Locate every Plasmodium parasite.
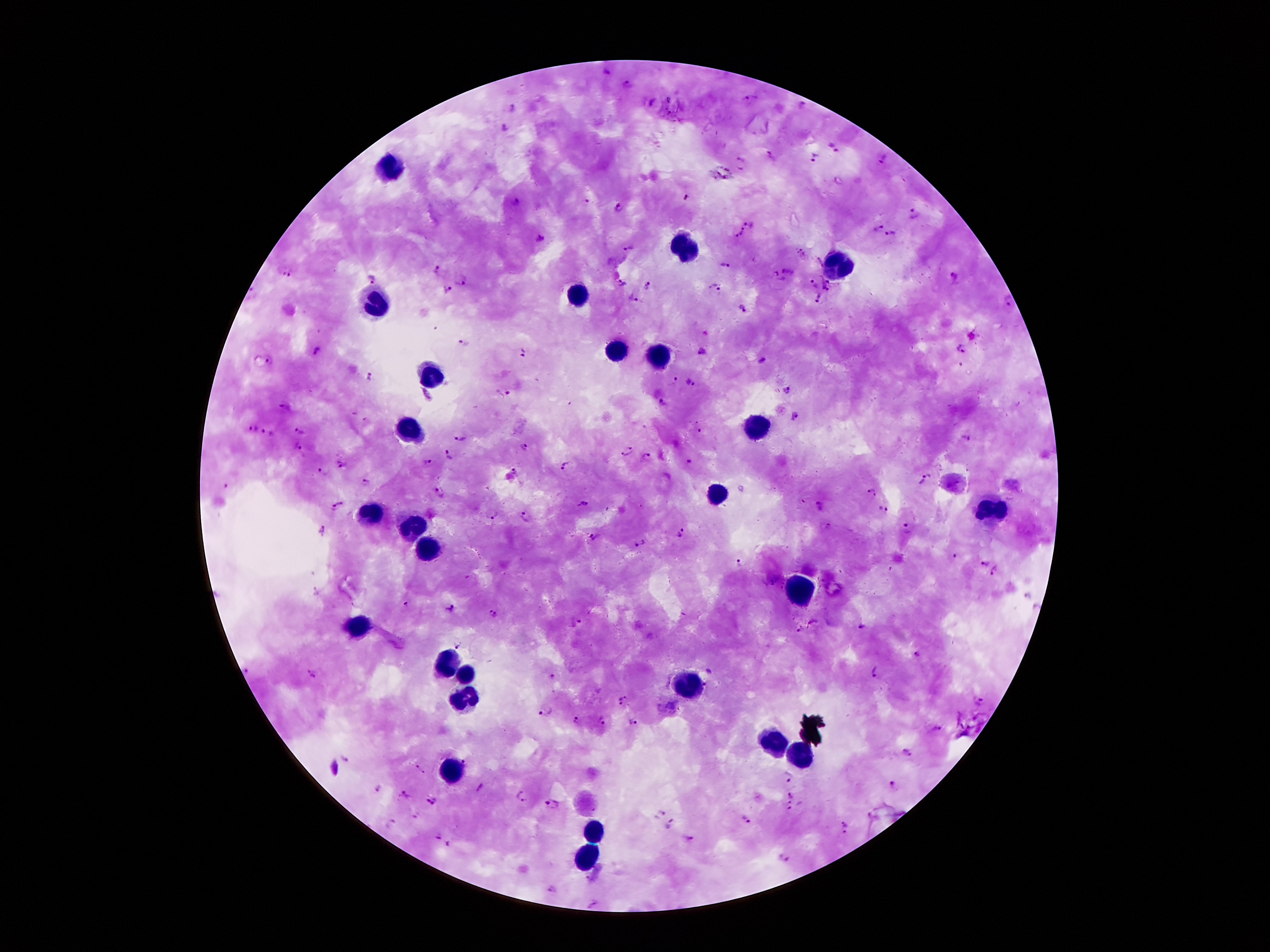

Approximate object centers, in pixels from the top-left corner.
Plasmodium parasites: (x=606, y=74), (x=627, y=85), (x=752, y=101), (x=511, y=107), (x=802, y=107), (x=504, y=127), (x=832, y=147), (x=770, y=154), (x=741, y=158), (x=815, y=160), (x=884, y=161), (x=585, y=201), (x=514, y=202), (x=619, y=209), (x=913, y=213), (x=750, y=225), (x=879, y=228), (x=741, y=233), (x=890, y=235), (x=538, y=238), (x=628, y=245), (x=723, y=267), (x=438, y=271), (x=284, y=273), (x=954, y=277), (x=779, y=278), (x=371, y=279), (x=461, y=281), (x=824, y=281), (x=621, y=282), (x=647, y=284), (x=812, y=284), (x=716, y=286), (x=448, y=290), (x=824, y=292), (x=634, y=299), (x=819, y=301), (x=1009, y=302), (x=744, y=307), (x=465, y=344), (x=963, y=349), (x=316, y=352), (x=701, y=352), (x=519, y=354), (x=269, y=362), (x=762, y=363), (x=371, y=378), (x=675, y=381), (x=691, y=384), (x=787, y=389), (x=502, y=391), (x=283, y=405), (x=356, y=412), (x=795, y=415), (x=367, y=422), (x=252, y=430), (x=300, y=432), (x=266, y=434), (x=459, y=438), (x=967, y=438), (x=633, y=446), (x=297, y=447), (x=526, y=447), (x=624, y=455), (x=449, y=456), (x=645, y=457), (x=427, y=463), (x=687, y=463), (x=340, y=464), (x=566, y=468), (x=516, y=470), (x=322, y=471), (x=925, y=479), (x=366, y=481), (x=440, y=492), (x=872, y=493), (x=342, y=501), (x=583, y=504), (x=822, y=505), (x=332, y=508), (x=883, y=509), (x=492, y=516), (x=526, y=516), (x=909, y=527), (x=323, y=532), (x=679, y=534), (x=594, y=536), (x=642, y=543), (x=955, y=557), (x=987, y=563), (x=739, y=566), (x=995, y=571), (x=405, y=605), (x=451, y=608), (x=493, y=616), (x=580, y=622), (x=814, y=622), (x=860, y=627), (x=797, y=629), (x=461, y=645), (x=916, y=653), (x=246, y=671), (x=877, y=672), (x=313, y=673), (x=551, y=677), (x=705, y=683), (x=622, y=700), (x=980, y=700), (x=545, y=711), (x=601, y=721), (x=576, y=722), (x=633, y=723), (x=936, y=727), (x=906, y=754), (x=346, y=759), (x=466, y=762), (x=421, y=769), (x=787, y=776), (x=378, y=787), (x=893, y=787), (x=479, y=788), (x=404, y=794), (x=791, y=795), (x=522, y=797), (x=434, y=802), (x=552, y=806), (x=790, y=810), (x=661, y=812), (x=747, y=821), (x=845, y=822), (x=389, y=823), (x=669, y=825), (x=843, y=833), (x=438, y=837), (x=691, y=839), (x=448, y=844), (x=784, y=860), (x=587, y=879), (x=551, y=890), (x=592, y=904).

Leukocyte locations: (x=393, y=171), (x=687, y=249), (x=838, y=265), (x=578, y=295), (x=378, y=309), (x=612, y=352), (x=654, y=354), (x=433, y=373), (x=758, y=425), (x=410, y=429), (x=716, y=498), (x=994, y=511), (x=372, y=515), (x=412, y=530), (x=425, y=551), (x=801, y=589), (x=360, y=629), (x=448, y=662), (x=469, y=673), (x=691, y=688), (x=465, y=700), (x=773, y=738), (x=803, y=759), (x=450, y=770), (x=595, y=835), (x=588, y=858). Giemsa-stained preparation. Thick blood film. Single field of view. 100x magnification. Patient malaria status: positive for Plasmodium falciparum. Image is 1270×952 pixels. Photographed through the microscope eyepiece with a smartphone camera.